Evaluate for Plasmodium parasites.
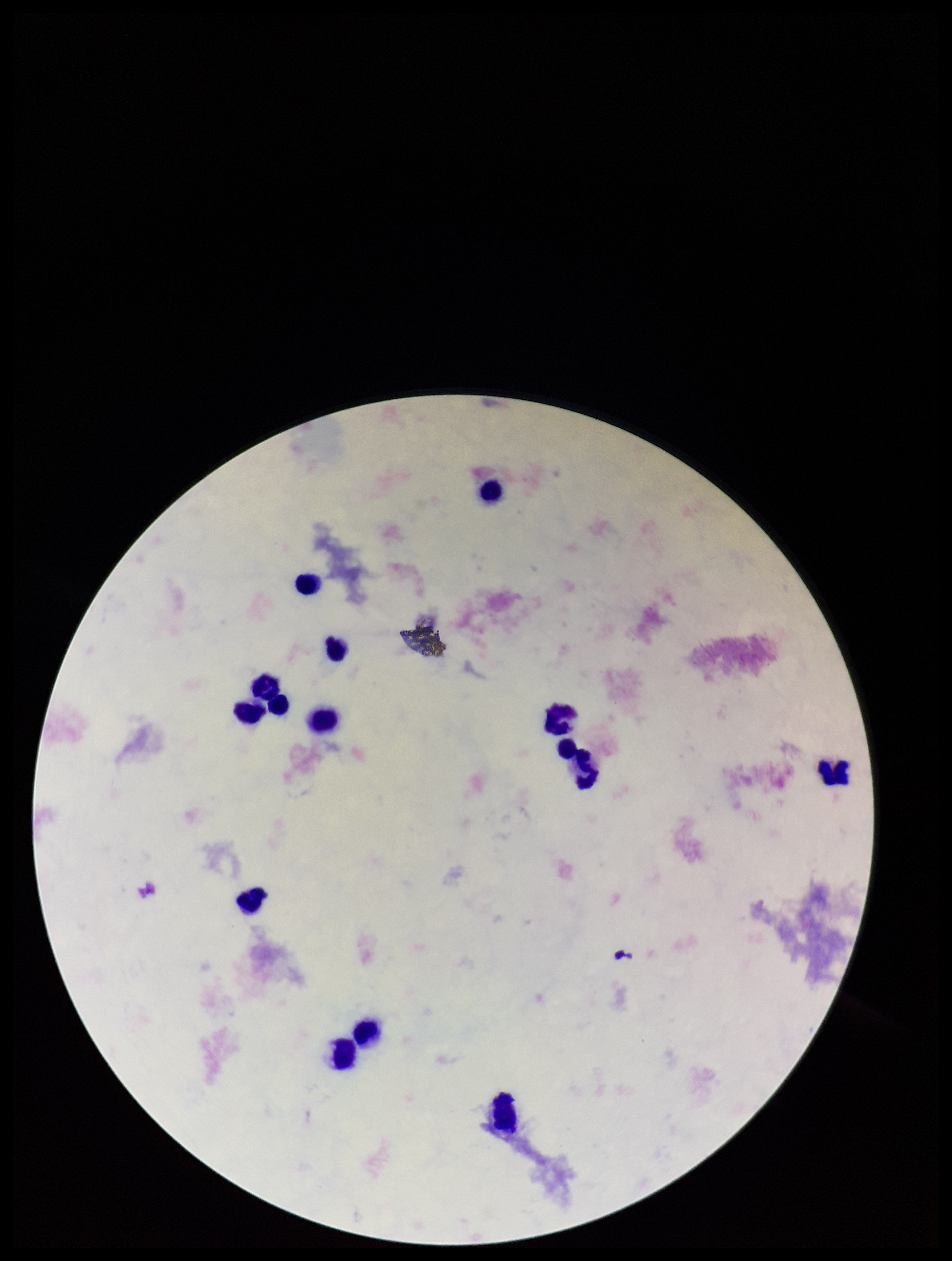
None identified.

Patient malaria status: negative. Smartphone photograph taken through the eyepiece of a microscope. Single field of view. Parasite count: 0. Giemsa stain. Leukocyte count: 13. Preparation: thick blood smear. Image is 952×1261 pixels.